Point out leukocytes.
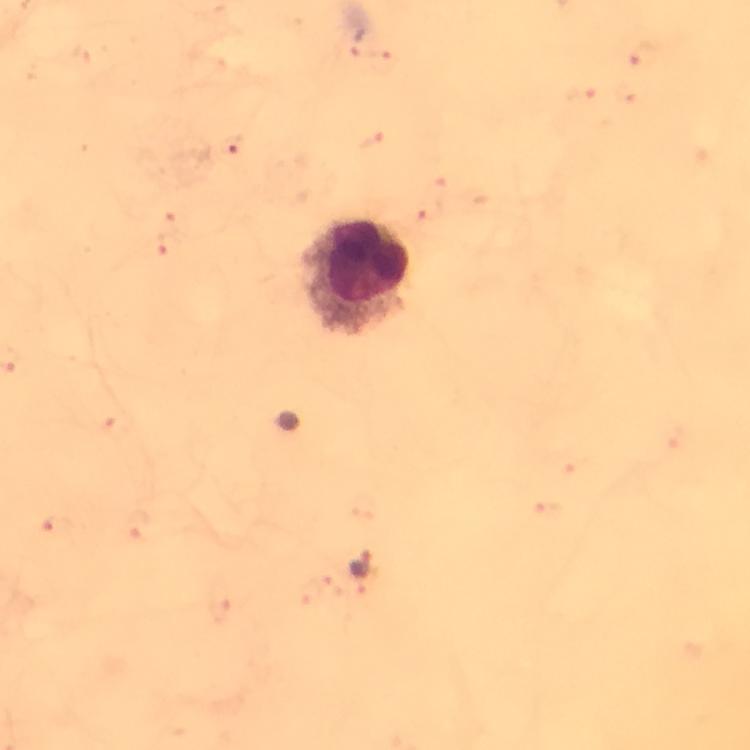

Approximate centers as [x, y] in pixels.
Leukocytes: [357, 276].

Summary:
  - Malaria parasite locations: [361, 564]
  - Capture: smartphone camera through the microscope
  - Preparation: thick blood smear
  - Context: from a malaria diagnostic workup
  - Image size: 750×750 pixels
  - Cropped from: a single field of view
  - Stain: Giemsa
  - Immersion oil: applied
  - Magnification: 100x